Assess this cell for malaria.
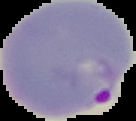
Parasitized.

Image is 136×121 pixels. From a thin blood film. Cell region segmented out of the field of view; the surrounding area is masked to black.